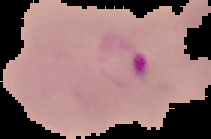

{
  "malaria_status": "parasitized",
  "preparation": "thin blood film",
  "image_size": "211×139 pixels",
  "image_type": "cell region segmented out of the field of view; surrounding area masked to black"
}